Report the malaria status of this cell.
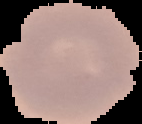

Uninfected.

Cell region segmented out of the field of view; the surrounding area is masked to black. Image is 142×124 pixels. From a thin blood film.